Assess this cell for malaria.
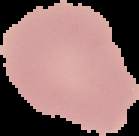

Uninfected.

Summary:
  - Image size: 139×136 pixels
  - Image type: cell region segmented out of the field of view; surrounding area masked to black
  - Preparation: thin blood smear